Classify this cell by malaria status.
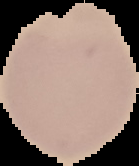
Uninfected.

image size = 139×166 pixels
preparation = thin blood film
image type = segmented cell region with the area outside set to black